Classify this cell by malaria status.
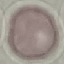
Uninfected.

stain = Giemsa
image type = cell patch, automatically extracted from a larger field of view and resized to 64 × 64 pixels
capture = smartphone camera at the microscope eyepiece
preparation = thin blood smear